Identify the parasite.
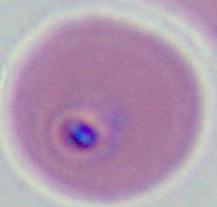

Plasmodium.

Micrograph. 400x or 1000x magnification.